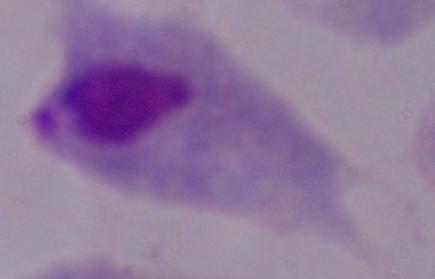
Summary:
  - Identification: trichomonad
  - Modality: micrograph
  - Magnification: 1000x